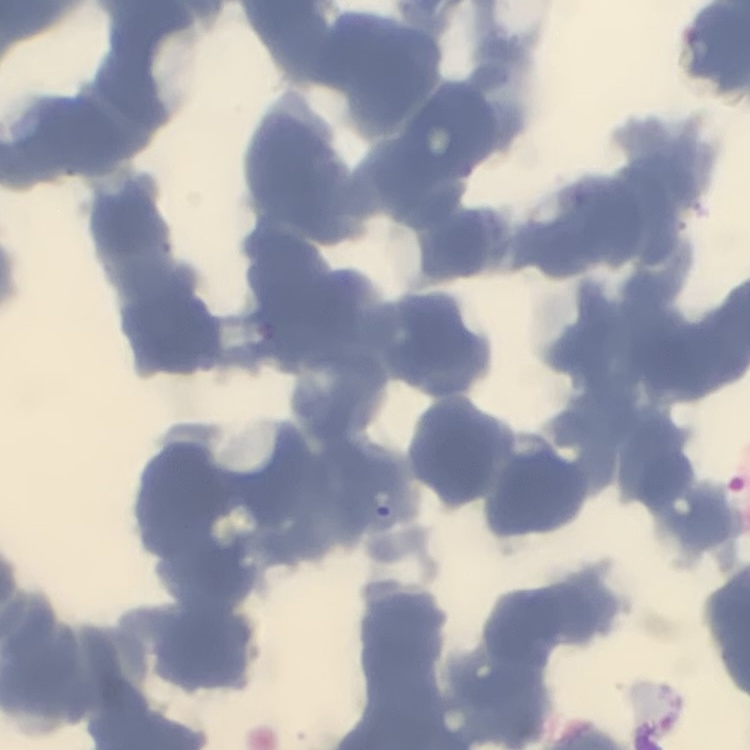
erythrocyte_morphology: rouleaux formation
preparation: thin blood film
image_type: square crop of a larger photomicrograph
stain: Field's or Giemsa